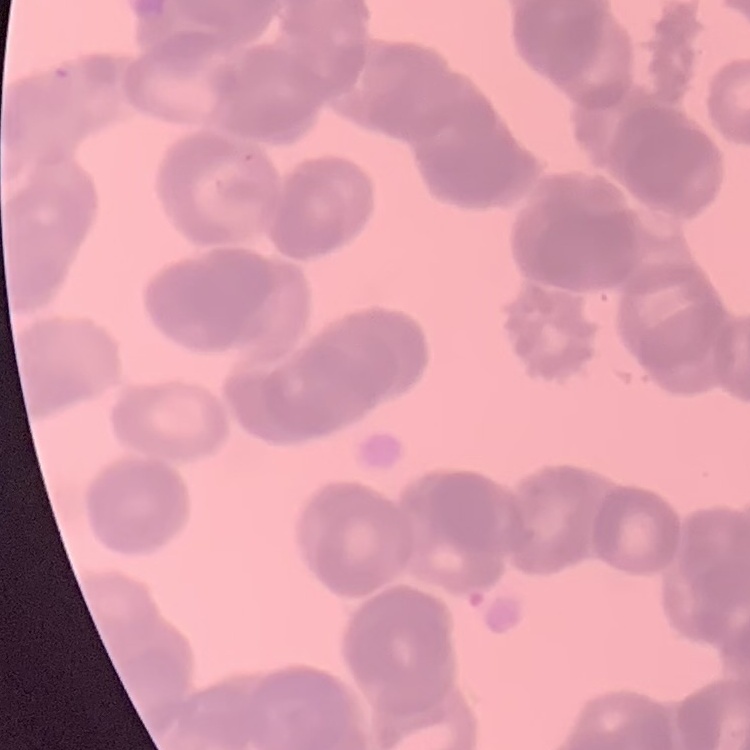

Summary:
  - Red blood cell morphology: rouleaux formation
  - Image type: one tile cut from a larger photomicrograph
  - Preparation: thin blood film
  - Stain: Field's or Giemsa